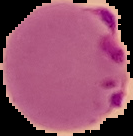 From a thin blood smear. Segmented cell region on a black background. Image is 133×136 pixels. Result: malaria parasites identified.